Give the extent of all Trypanosoma brucei.
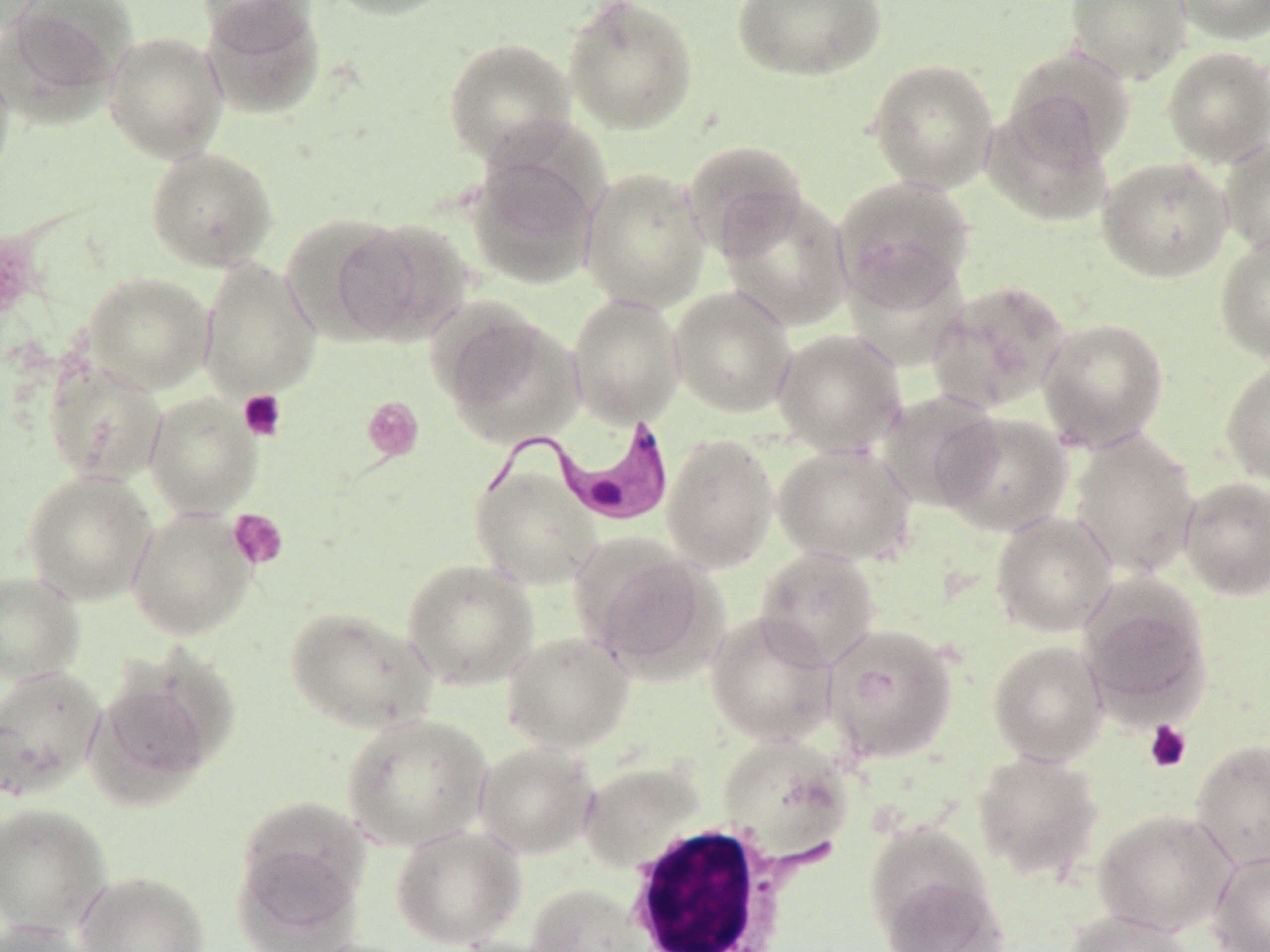
Approximate bounding boxes as (x1,y1)-(x2,y2) corner pairs in pixels.
Trypanosoma brucei: (471,413)-(676,528).

Uninfected red blood cell locations: (1,0)-(134,117), (195,0)-(321,48), (321,0)-(458,21), (562,0)-(698,135), (732,0)-(885,82), (1065,0)-(1191,84), (1170,0)-(1270,45), (202,2)-(326,119), (103,31)-(228,162), (443,37)-(578,166), (1004,45)-(1136,165), (1162,46)-(1270,167), (0,56)-(15,188), (867,58)-(999,192), (981,101)-(1116,228), (1220,137)-(1270,258), (682,139)-(809,258), (145,146)-(279,271), (466,152)-(601,288), (1096,156)-(1234,283), (580,167)-(711,312), (833,174)-(976,311), (716,190)-(854,331), (280,213)-(417,341), (331,217)-(474,344), (1214,234)-(1270,361), (198,258)-(321,398), (83,272)-(214,394), (927,278)-(1072,414), (668,286)-(797,418), (566,293)-(685,427), (436,308)-(584,447), (1037,316)-(1170,450), (772,328)-(907,457), (43,360)-(166,486), (1220,360)-(1270,487), (876,390)-(1004,511), (144,392)-(262,518), (937,412)-(1073,537), (1068,430)-(1201,580), (662,434)-(779,572), (773,442)-(918,566), (470,463)-(602,590), (22,469)-(157,606), (1178,476)-(1270,600), (125,507)-(257,640), (991,510)-(1118,637), (754,546)-(882,670), (583,547)-(722,678), (401,557)-(538,690), (0,570)-(85,685), (1077,578)-(1212,720), (284,605)-(436,734), (705,610)-(837,746), (823,622)-(959,765), (501,631)-(635,754), (988,640)-(1109,766), (0,664)-(107,802), (84,671)-(218,808), (342,713)-(492,852), (717,733)-(854,863), (1189,739)-(1270,871), (474,742)-(599,859), (972,749)-(1103,882), (578,759)-(706,874), (0,803)-(112,936), (1093,808)-(1238,937), (232,812)-(369,947), (390,825)-(526,950), (1209,849)-(1270,952), (74,871)-(210,952), (878,873)-(1010,952), (525,883)-(648,952), (1062,909)-(1195,952), (0,919)-(94,952), (445,937)-(563,952). White blood cell locations: (620,822)-(826,951). Platelet locations: (0,229)-(42,322), (238,389)-(287,440), (362,396)-(423,461), (228,508)-(288,570), (1143,720)-(1192,773). Slide-level diagnosis: Trypanosoma brucei. Image is 1270×952 pixels. Single field of view. May-Grünwald-Giemsa-stained preparation. Captured at 1000x magnification. Thin blood film. Optical microscopy.